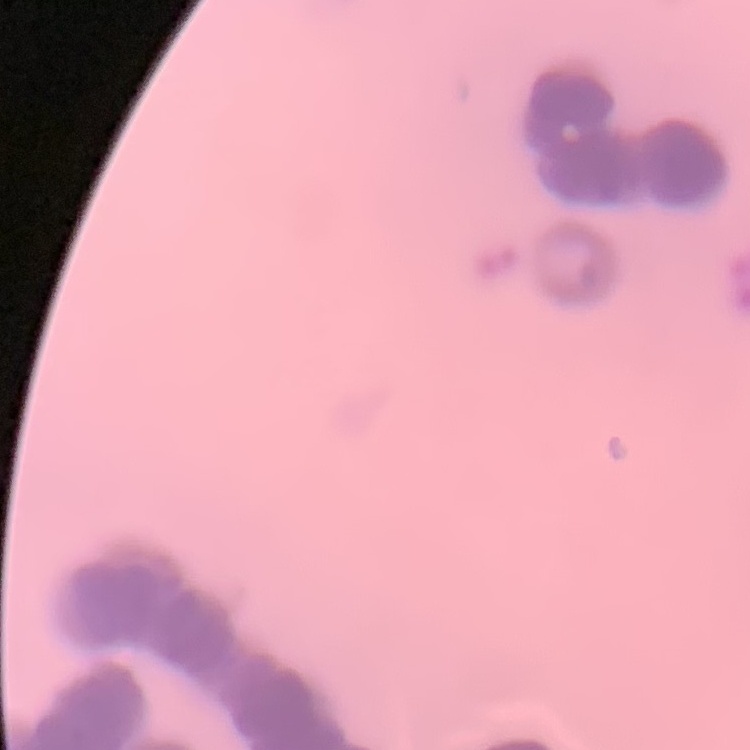

Summary:
  - Red blood cell morphology: rouleaux formation
  - Preparation: thin blood film
  - Stain: Field's or Giemsa
  - Image type: square crop of a larger photomicrograph